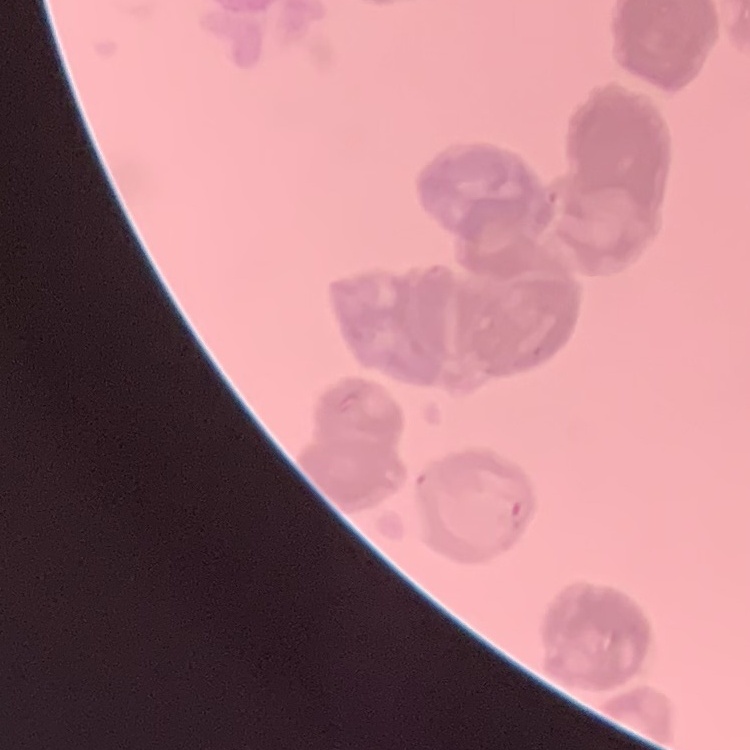

Summary:
  - Red blood cell morphology: rouleaux formation
  - Preparation: thin blood smear
  - Stain: Field's or Giemsa
  - Image type: square crop of a larger photomicrograph